Give the extent of all Plasmodium vivax-infected red blood cells.
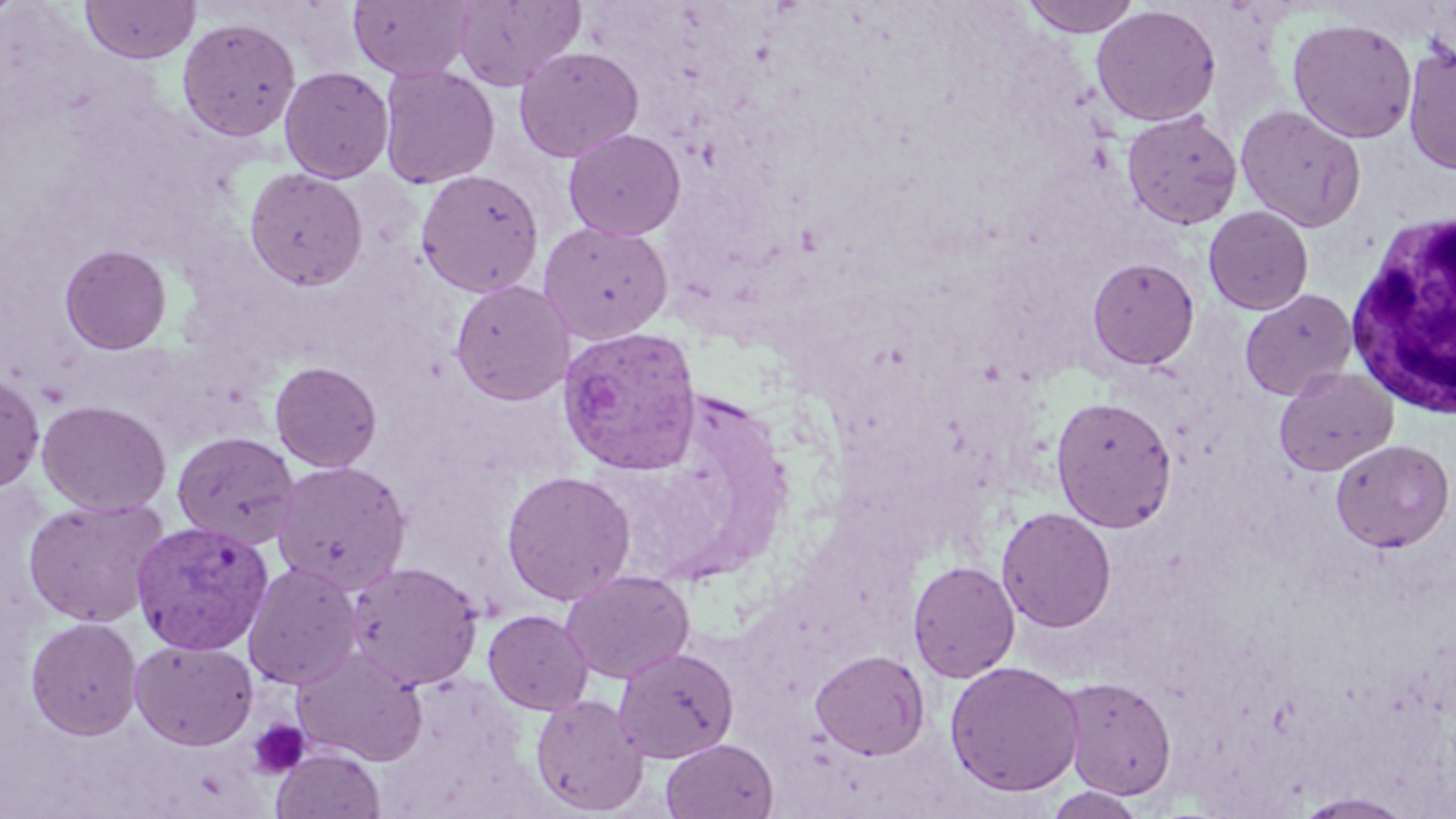
Approximate bounding boxes as (x1,y1)-(x2,y2) corner pairs in pixels.
Plasmodium vivax-infected red blood cells: (557,325)-(703,476), (131,519)-(274,654).

Summary:
  - Uninfected red blood cell locations: (349,0)-(474,81), (452,0)-(585,90), (1018,0)-(1143,37), (81,1)-(200,64), (1091,4)-(1222,126), (177,16)-(300,142), (1287,17)-(1417,143), (1402,41)-(1456,176), (514,46)-(644,162), (378,64)-(499,189), (279,66)-(394,183), (1235,104)-(1367,232), (1122,110)-(1243,230), (563,128)-(686,241), (244,167)-(367,290), (416,169)-(544,297), (1204,206)-(1314,315), (538,221)-(673,344), (59,243)-(172,354), (1087,256)-(1200,370), (450,279)-(575,405), (1240,289)-(1358,400), (270,361)-(383,472), (1274,366)-(1398,476), (0,372)-(45,493), (1050,395)-(1177,532), (36,399)-(172,517), (172,431)-(299,550), (1331,438)-(1455,552), (271,459)-(411,595), (501,470)-(636,605), (23,497)-(169,627), (996,506)-(1117,633), (908,560)-(1021,683), (347,561)-(484,690), (242,562)-(362,690), (561,569)-(695,684), (483,610)-(593,714), (25,616)-(143,739), (129,639)-(259,751), (613,645)-(740,763), (292,647)-(427,765), (810,649)-(930,760), (945,660)-(1084,797), (1059,676)-(1177,800), (530,693)-(649,816), (660,738)-(779,819), (272,747)-(385,819), (1044,787)-(1149,818), (1293,791)-(1417,818)
  - Platelet locations: (248,719)-(310,779)
  - White blood cell locations: (1346,206)-(1455,420)
  - Slide-level diagnosis: Plasmodium vivax
  - Magnification: 1000x
  - Stain: May-Grünwald-Giemsa
  - Image size: 1456×819 pixels
  - Field of view: single
  - Modality: optical microscopy
  - Preparation: thin blood smear